State which parasite is depicted.
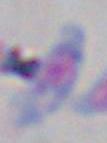
Toxoplasma gondii.

magnification: 1000x
modality: photomicrograph